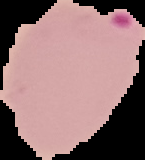 The area outside the segmented cell region is set to black. From a thin blood smear. Malaria status: parasitized. Image is 145×160 pixels.